Give the position of every malaria parasite.
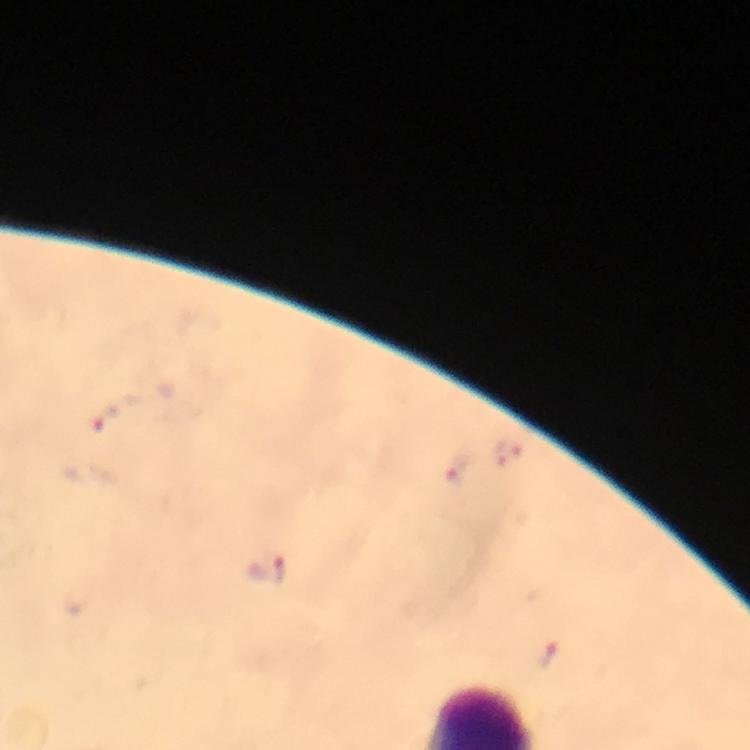

Approximate centers as {x, y} in pixels.
Malaria parasites: {104, 418}, {510, 454}, {460, 467}, {267, 570}, {548, 654}.

Image is 750×750 pixels. From a diagnostic examination for malaria. A crop from one field of view. Giemsa stain. Immersion oil applied. Smartphone photograph taken through a microscope. At 100x magnification. Thick blood film.